Classify this cell by malaria status.
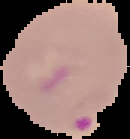
Parasitized.

Summary:
  - Image type: cell region segmented out of the field of view; surrounding area masked to black
  - Preparation: thin blood smear
  - Image size: 130×139 pixels